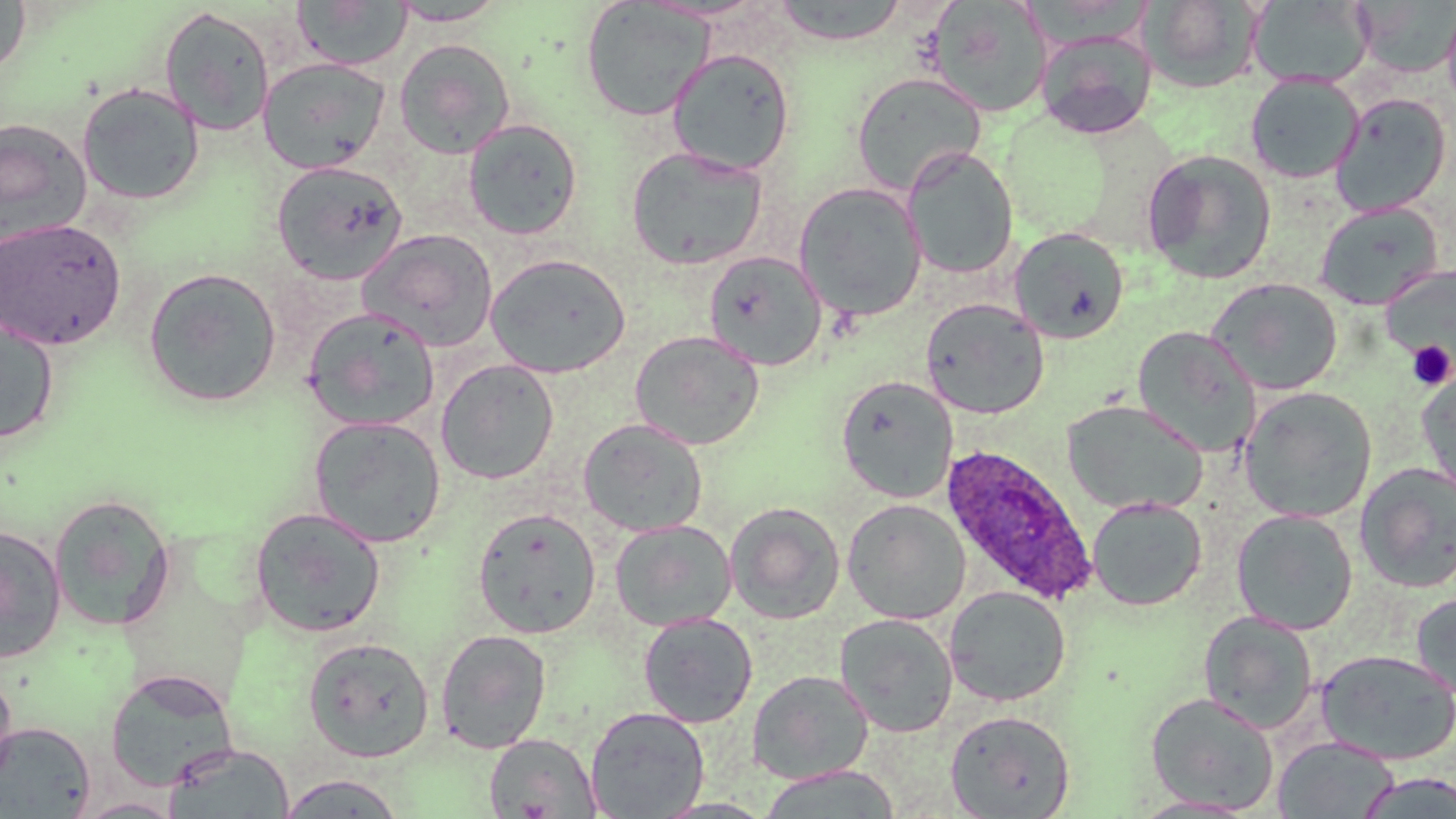
slide-level diagnosis = Plasmodium ovale
magnification = 1000x
Plasmodium ovale-infected red blood cell locations = approximate bounding boxes as (x1,y1)-(x2,y2) corner pairs in pixels: (940,444)-(1096,607)
stain = May-Grünwald-Giemsa
preparation = thin blood smear
field of view = single
modality = light microscopy
uninfected red blood cell locations = approximate bounding boxes as (x1,y1)-(x2,y2) corner pairs in pixels: (0,0)-(32,79), (1144,0)-(1263,94), (294,1)-(412,70), (580,1)-(715,121), (772,1)-(910,46), (927,1)-(1053,119), (1249,1)-(1374,89), (1353,1)-(1456,79), (389,2)-(508,26), (1442,2)-(1456,117), (159,6)-(275,137), (1036,29)-(1157,139), (394,39)-(515,159), (667,48)-(795,176), (258,57)-(390,174), (851,71)-(987,196), (1245,74)-(1364,184), (76,82)-(205,205), (1330,93)-(1452,217), (463,118)-(583,240), (0,119)-(93,247), (625,145)-(768,270), (901,145)-(1018,280), (1141,149)-(1277,285), (270,160)-(409,285), (793,181)-(928,322), (1314,201)-(1442,309), (0,217)-(127,350), (1009,227)-(1129,343), (358,228)-(498,352), (703,250)-(827,371), (485,253)-(632,378), (1382,266)-(1455,370), (142,267)-(282,408), (1207,277)-(1342,395), (920,298)-(1050,419), (302,307)-(441,431), (0,316)-(60,444), (1131,326)-(1260,456), (629,330)-(765,450), (435,359)-(560,485), (1417,368)-(1456,504), (835,374)-(958,503), (1240,386)-(1377,523), (1061,399)-(1208,517), (308,415)-(447,548), (578,418)-(709,537), (1354,461)-(1456,593), (48,493)-(176,631), (1086,497)-(1207,611), (842,498)-(971,625), (725,501)-(846,624), (249,507)-(387,638), (472,507)-(601,638), (1231,509)-(1358,635), (610,519)-(737,632), (0,525)-(67,663), (944,585)-(1071,706), (1410,590)-(1456,704), (1197,610)-(1320,734), (638,612)-(758,728), (834,613)-(959,737), (435,628)-(553,754), (303,636)-(435,762), (1315,648)-(1456,765), (104,668)-(239,791), (747,669)-(874,785), (0,670)-(18,788), (1145,691)-(1280,814), (585,706)-(710,818), (945,709)-(1076,819), (0,720)-(96,817), (485,732)-(601,817), (1272,735)-(1399,818), (163,742)-(296,819), (757,765)-(902,819), (277,773)-(407,818), (1128,795)-(1260,818), (73,796)-(185,818)
image size = 1456×819 pixels
platelet locations = approximate bounding boxes as (x1,y1)-(x2,y2) corner pairs in pixels: (1407,340)-(1454,390)